Classify this cell by malaria status.
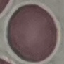

Uninfected.

Thin smear of blood. Automatically extracted cell patch, resized to 64 × 64 pixels. Giemsa stain. Photographed with a smartphone camera at the microscope eyepiece.